Assess this cell for malaria.
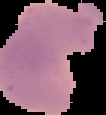
It is parasitized.

image type = segmented cell region with the area outside set to black
image size = 106×115 pixels
preparation = thin blood film